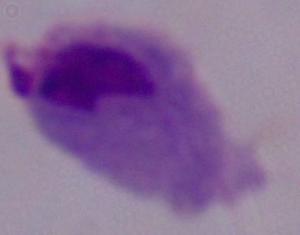
Micrograph. Captured at 1000x magnification. A trichomonad is shown.